Report the malaria status of this cell.
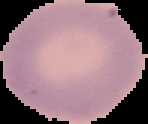

It is uninfected.

Segmented cell region on a black background. From a thin blood smear. Image is 148×124 pixels.